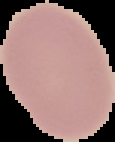
image size = 115×142 pixels
preparation = thin blood smear
result = no Plasmodium parasites detected
image type = cell region segmented out of the field of view; surrounding area masked to black